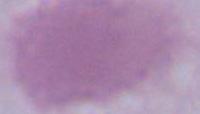

magnification: 1000x
modality: photomicrograph
identification: erythrocyte